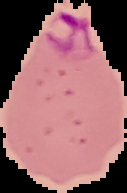 Cell region segmented out of the field of view; the surrounding area is masked to black. Malaria status: parasitized. Image is 127×193 pixels. From a thin blood film.